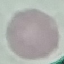
Summary:
  - Result: negative for malaria parasites
  - Preparation: thin blood film
  - Image type: automatically extracted cell patch, resized to 64 × 64 pixels
  - Stain: Giemsa
  - Capture: smartphone through the microscope eyepiece